Outline each uninfected red blood cell.
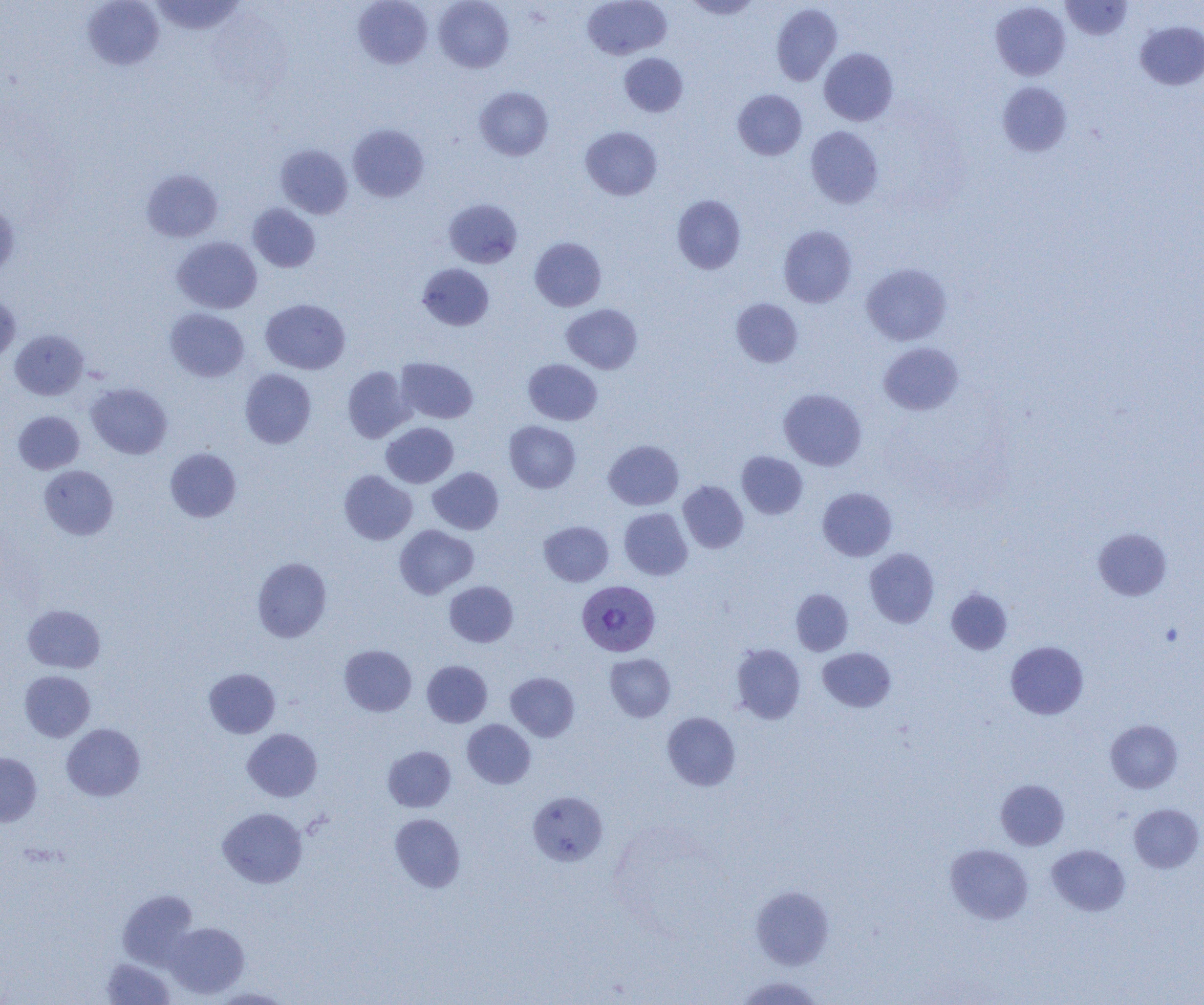
Approximate bounding boxes as (x1,y1)-(x2,y2) corner pairs in pixels.
Uninfected red blood cells: (82,0)-(164,71), (149,0)-(245,35), (353,0)-(432,69), (434,0)-(514,72), (582,0)-(671,60), (683,0)-(762,19), (1061,1)-(1132,40), (990,2)-(1070,80), (771,3)-(842,85), (1135,21)-(1204,90), (819,48)-(898,126), (619,53)-(688,117), (997,81)-(1072,157), (474,86)-(553,160), (733,89)-(807,160), (348,124)-(429,202), (805,125)-(883,208), (581,126)-(662,200), (275,144)-(353,219), (141,169)-(222,242), (672,195)-(746,274), (443,199)-(522,268), (0,201)-(19,277), (248,203)-(320,272), (779,225)-(856,308), (172,236)-(262,314), (530,237)-(606,311), (417,263)-(494,331), (861,263)-(952,345), (0,292)-(21,366), (731,298)-(802,367), (260,299)-(350,374), (561,304)-(642,373), (165,308)-(249,382), (10,330)-(89,400), (879,342)-(963,415), (396,357)-(478,423), (523,359)-(602,425), (342,366)-(413,442), (240,369)-(316,448), (86,383)-(172,459), (779,388)-(866,470), (13,410)-(85,474), (504,421)-(580,493), (381,422)-(458,488), (604,440)-(683,510), (165,448)-(241,522), (737,451)-(807,519), (39,465)-(118,540), (428,467)-(504,534), (339,470)-(417,545), (678,481)-(748,553), (817,487)-(897,561), (619,508)-(693,580), (539,521)-(613,586), (394,525)-(478,599), (1093,528)-(1172,601), (864,548)-(939,627), (252,557)-(332,642), (444,581)-(518,647), (946,588)-(1013,654), (791,589)-(853,656), (23,604)-(105,673), (1006,641)-(1088,719), (339,644)-(417,716), (730,644)-(806,724), (818,647)-(896,712), (605,653)-(676,721), (422,660)-(492,727), (204,668)-(280,738), (20,670)-(95,742), (506,672)-(579,741), (662,712)-(740,791), (462,719)-(536,788), (1105,719)-(1182,793), (62,723)-(145,801), (242,729)-(322,801), (383,746)-(456,812), (0,752)-(42,826), (996,779)-(1069,850), (528,791)-(608,866), (1129,803)-(1203,873), (218,807)-(307,887), (389,813)-(465,892), (945,844)-(1033,924), (1046,844)-(1130,916), (749,885)-(834,970), (117,890)-(198,969), (165,922)-(249,999), (102,958)-(175,1004), (734,976)-(823,1004), (211,988)-(293,1004).

Summary:
  - Plasmodium vivax-infected red blood cell locations: (577,580)-(660,657)
  - Slide-level diagnosis: Plasmodium vivax
  - Preparation: thin blood smear
  - Magnification: 1000x
  - Image size: 1204×1005 pixels
  - Modality: light microscopy
  - Field of view: single